Locate every blood parasite and identify its species.
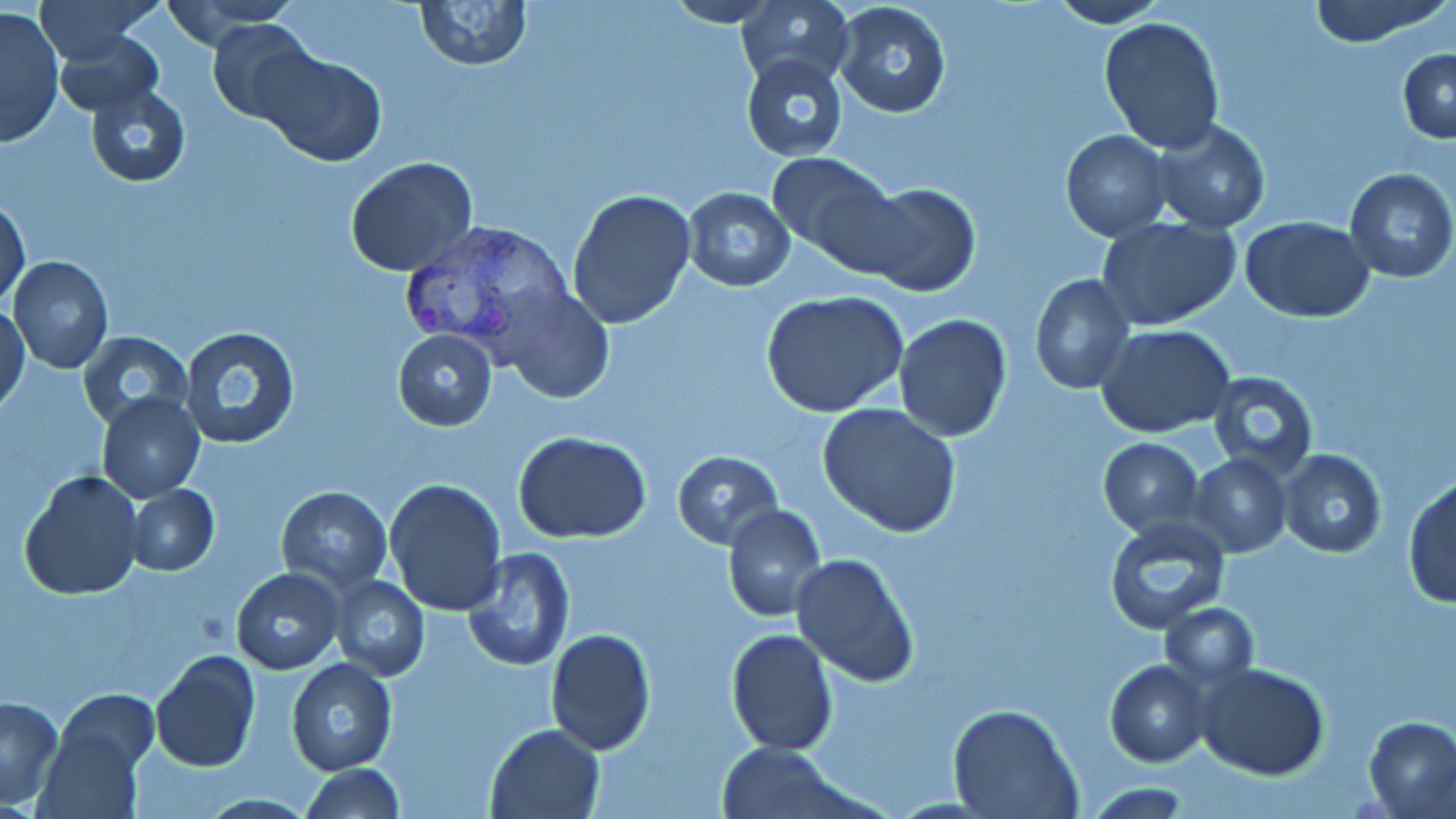

Approximate bounding boxes as (x1, y1, x2, y2) in pixels.
Plasmodium vivax-infected red blood cells: (393, 220, 574, 362).
No Plasmodium falciparum, Plasmodium ovale, Plasmodium malariae, Babesia divergens, or Trypanosoma brucei observed.

Uninfected red blood cell locations: (37, 0, 160, 63), (414, 0, 531, 70), (662, 0, 783, 27), (736, 0, 854, 88), (1049, 0, 1168, 27), (1307, 0, 1447, 48), (157, 1, 304, 40), (831, 1, 953, 119), (0, 8, 64, 147), (205, 17, 323, 124), (1098, 17, 1225, 156), (53, 29, 164, 117), (1398, 49, 1456, 143), (256, 50, 387, 168), (741, 54, 849, 161), (84, 84, 192, 186), (1150, 119, 1273, 235), (1061, 130, 1171, 241), (765, 152, 900, 267), (345, 156, 480, 276), (1343, 169, 1456, 282), (857, 183, 979, 297), (681, 185, 795, 291), (566, 189, 696, 330), (1, 198, 30, 307), (1241, 216, 1375, 322), (1098, 217, 1242, 331), (8, 254, 114, 374), (1029, 273, 1136, 394), (500, 283, 616, 400), (761, 290, 909, 418), (1, 303, 29, 414), (894, 315, 1012, 441), (1095, 323, 1235, 439), (178, 325, 302, 450), (76, 329, 194, 431), (391, 330, 497, 431), (1205, 370, 1318, 478), (97, 391, 205, 501), (818, 403, 961, 538), (513, 430, 654, 543), (1098, 438, 1204, 537), (673, 450, 783, 548), (1278, 450, 1386, 559), (1189, 453, 1290, 557), (18, 470, 145, 599), (384, 477, 508, 615), (1404, 477, 1456, 608), (125, 485, 220, 578), (277, 486, 391, 592), (721, 504, 826, 621), (1103, 515, 1230, 633), (461, 548, 576, 670), (791, 552, 920, 686), (230, 568, 343, 675), (328, 575, 431, 680), (1159, 603, 1259, 688), (545, 629, 657, 755), (725, 629, 838, 756), (150, 649, 260, 773), (286, 657, 397, 776), (1105, 660, 1211, 766), (1196, 662, 1330, 782), (53, 689, 159, 775), (0, 695, 64, 807), (948, 703, 1081, 818), (1365, 716, 1456, 816), (36, 722, 146, 819), (485, 723, 605, 818), (717, 741, 846, 816), (296, 764, 406, 819), (1081, 784, 1193, 815). Slide-level diagnosis: Plasmodium vivax. Single field of view. 1000x magnification. Thin blood smear. Image is 1456×819 pixels. Optical microscopy. May-Grünwald-Giemsa stain.